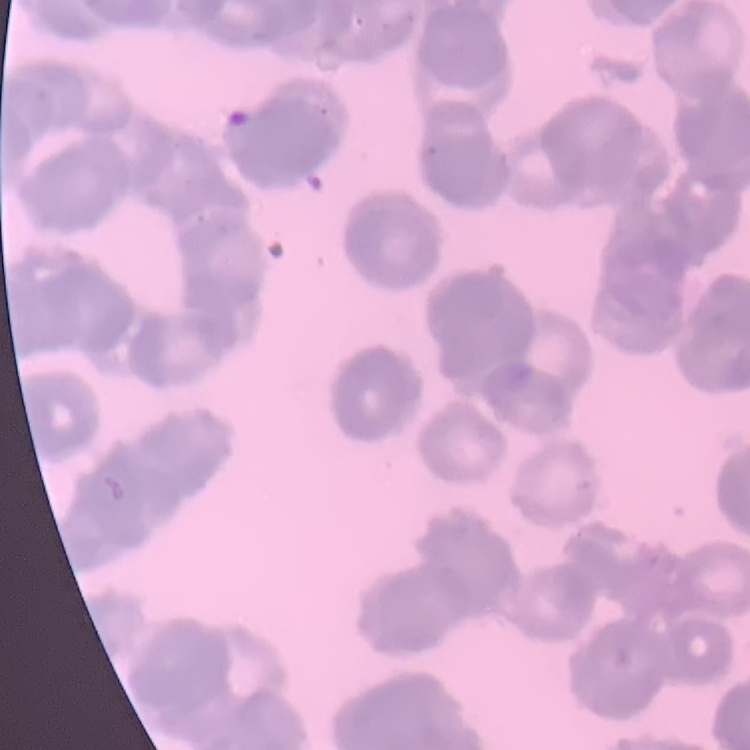
Summary:
  - Erythrocyte morphology: rouleaux formation
  - Preparation: thin blood smear
  - Image type: one tile cut from a larger photomicrograph
  - Stain: Field's or Giemsa